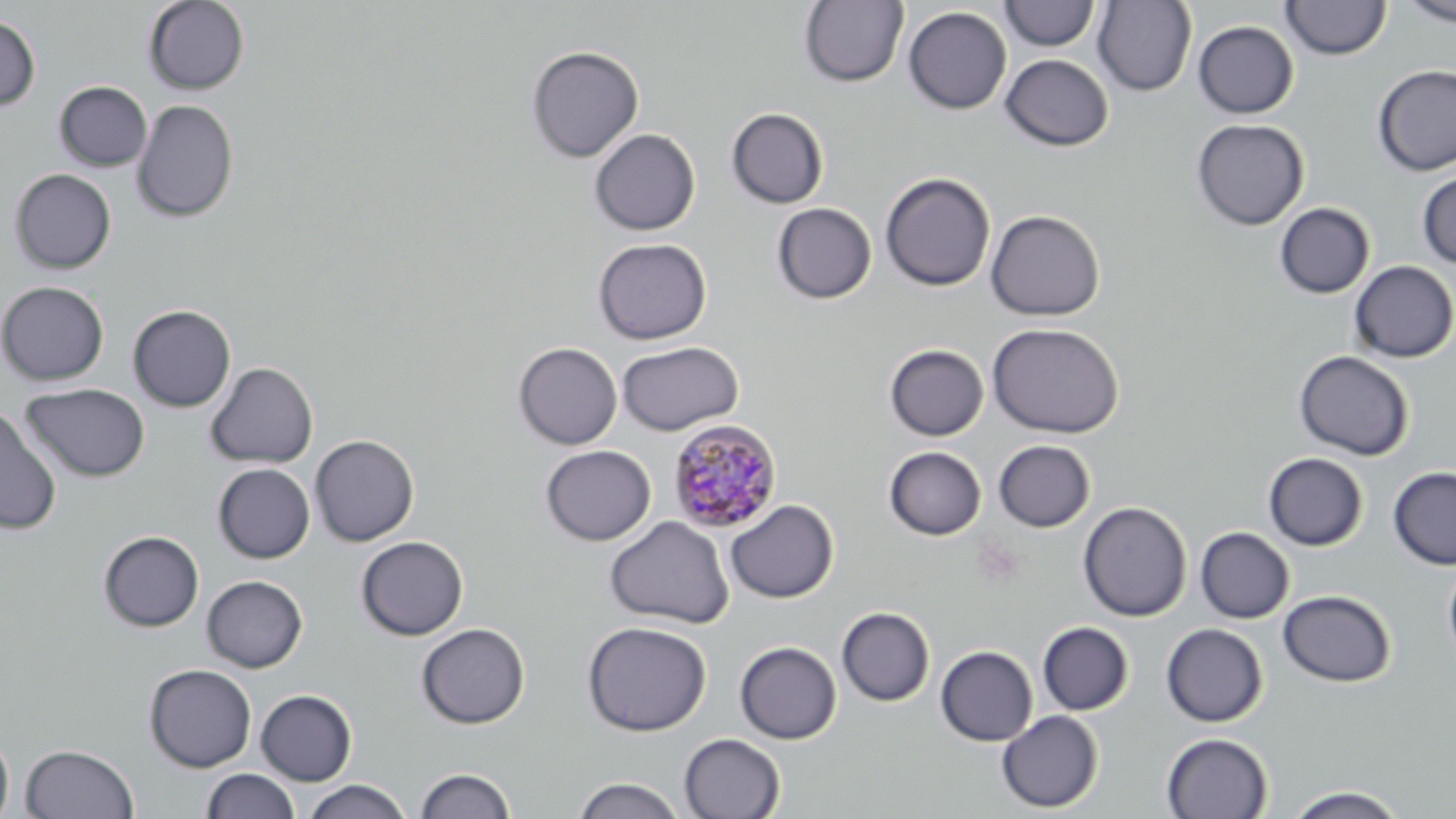

{
  "slide_level_diagnosis": "Plasmodium malariae",
  "stain": "May-Grünwald-Giemsa",
  "uninfected_red_blood_cell_locations": "approximate bounding boxes as (x1, y1, x2, y2) in pixels: (143, 0, 250, 95), (799, 0, 908, 87), (1399, 0, 1456, 26), (999, 1, 1099, 51), (1092, 1, 1197, 96), (1281, 1, 1391, 60), (903, 6, 1012, 114), (0, 15, 40, 111), (1193, 21, 1298, 118), (526, 45, 644, 163), (1000, 54, 1114, 151), (1373, 64, 1456, 176), (54, 81, 152, 171), (131, 99, 239, 223), (726, 107, 829, 208), (1191, 118, 1309, 230), (589, 128, 700, 235), (9, 168, 116, 274), (1417, 171, 1456, 269), (880, 172, 996, 292), (771, 203, 877, 304), (1274, 203, 1374, 298), (985, 209, 1105, 321), (593, 238, 712, 344), (1349, 261, 1456, 363), (0, 281, 109, 385), (128, 305, 236, 412), (987, 322, 1125, 438), (617, 341, 744, 435), (513, 342, 622, 450), (884, 344, 989, 441), (1293, 350, 1414, 461), (205, 362, 318, 469), (21, 383, 150, 482), (0, 405, 62, 535), (310, 435, 419, 546), (993, 440, 1095, 532), (540, 445, 655, 546), (883, 446, 986, 540), (1263, 452, 1369, 551), (211, 454, 415, 556), (213, 463, 315, 563), (1388, 466, 1456, 570), (724, 499, 838, 604), (1078, 501, 1192, 622), (604, 516, 735, 629), (1195, 527, 1295, 623), (98, 531, 204, 632), (356, 536, 468, 640), (1442, 561, 1456, 664), (202, 575, 308, 672), (1277, 589, 1396, 687), (837, 607, 935, 706), (582, 621, 711, 736), (1037, 622, 1134, 715), (416, 623, 530, 729), (1161, 623, 1268, 727), (735, 641, 842, 744), (935, 646, 1038, 746), (143, 663, 257, 772), (256, 689, 357, 785), (996, 710, 1104, 813), (0, 728, 14, 819), (679, 733, 785, 818), (1161, 733, 1273, 819), (21, 744, 139, 818), (415, 767, 516, 818), (201, 768, 300, 819), (571, 776, 686, 819), (303, 779, 413, 818), (1283, 786, 1409, 818)",
  "modality": "light microscopy",
  "preparation": "thin blood film",
  "plasmodium_malariae_infected_red_blood_cell_locations": "approximate bounding boxes as (x1, y1, x2, y2) in pixels: (668, 418, 783, 532)",
  "field_of_view": "single",
  "magnification": "1000x",
  "image_size": "1456×819 pixels"
}